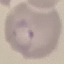
Summary:
  - Result: malaria parasites detected
  - Stain: Giemsa
  - Capture: smartphone camera at the microscope eyepiece
  - Preparation: thin blood smear
  - Image type: cell patch, automatically extracted from a larger field of view and resized to 64 × 64 pixels